Assess this cell for malaria.
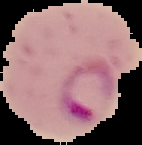

Parasitized.

Summary:
  - Image size: 142×145 pixels
  - Image type: cell region segmented out of the field of view; surrounding area masked to black
  - Preparation: thin blood film